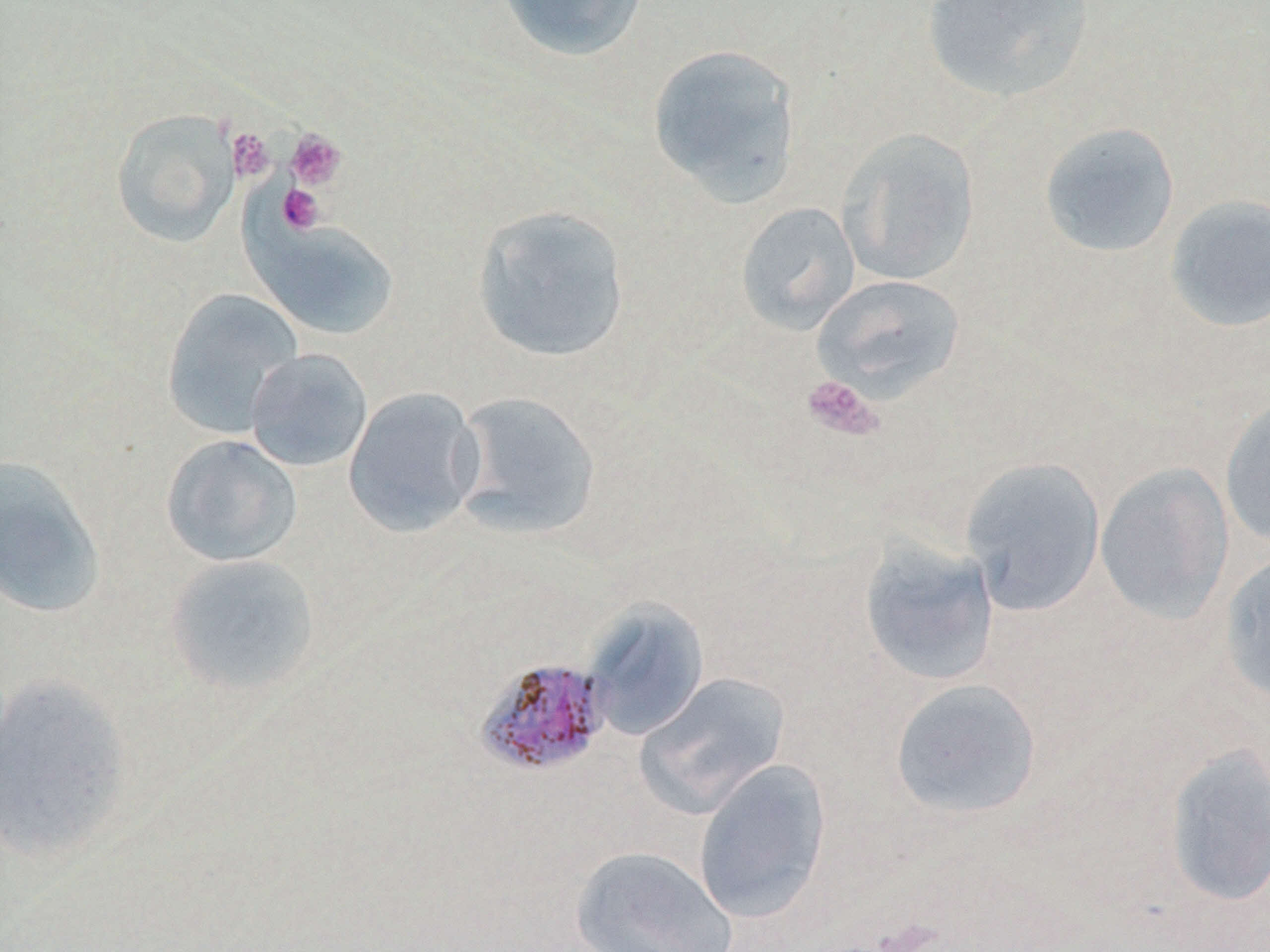

Summary:
  - Coordinate format: approximate bounding boxes as [x1, y1, x2, y2] in pixels
  - Uninfected red blood cell locations: [497, 0, 648, 62], [920, 1, 1095, 103], [647, 42, 803, 206], [111, 110, 239, 248], [1039, 121, 1181, 258], [837, 128, 979, 286], [1164, 194, 1270, 332], [735, 202, 860, 335], [471, 204, 631, 364], [248, 218, 400, 341], [812, 273, 966, 401], [160, 288, 304, 438], [244, 348, 373, 473], [342, 387, 485, 538], [450, 390, 602, 541], [1220, 395, 1270, 549], [160, 433, 302, 568], [0, 455, 106, 619], [959, 457, 1106, 616], [1094, 461, 1235, 625], [858, 538, 1001, 687], [1218, 551, 1270, 705], [163, 553, 322, 696], [582, 598, 710, 741], [634, 671, 791, 817], [0, 673, 137, 865], [889, 677, 1042, 821], [1162, 743, 1270, 908], [693, 758, 832, 925], [569, 845, 738, 952]
  - Platelet locations: [227, 128, 275, 183], [285, 128, 347, 191], [278, 183, 325, 235], [801, 375, 884, 441]
  - Plasmodium malariae-infected red blood cell locations: [474, 658, 613, 777]
  - Slide-level diagnosis: Plasmodium malariae
  - Stain: May-Grünwald-Giemsa
  - Preparation: thin blood film
  - Magnification: 1000x
  - Modality: optical microscopy
  - Field of view: single
  - Image size: 1270×952 pixels